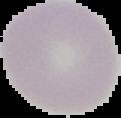 Malaria status: uninfected. Image is 121×118 pixels. Cell region segmented out of the field of view; the surrounding area is masked to black. From a thin blood film.